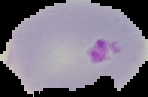 Image is 148×97 pixels. From a thin blood smear. Result: Plasmodium parasites identified. Cell region segmented out of the field of view; the surrounding area is masked to black.